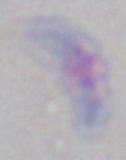
Summary:
  - Identification: Toxoplasma gondii
  - Modality: photomicrograph
  - Magnification: 1000x